Identify the parasite.
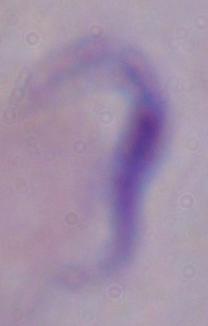
This is a trypanosome.

Photomicrograph. 1000x magnification.